Outline every Plasmodium parasite.
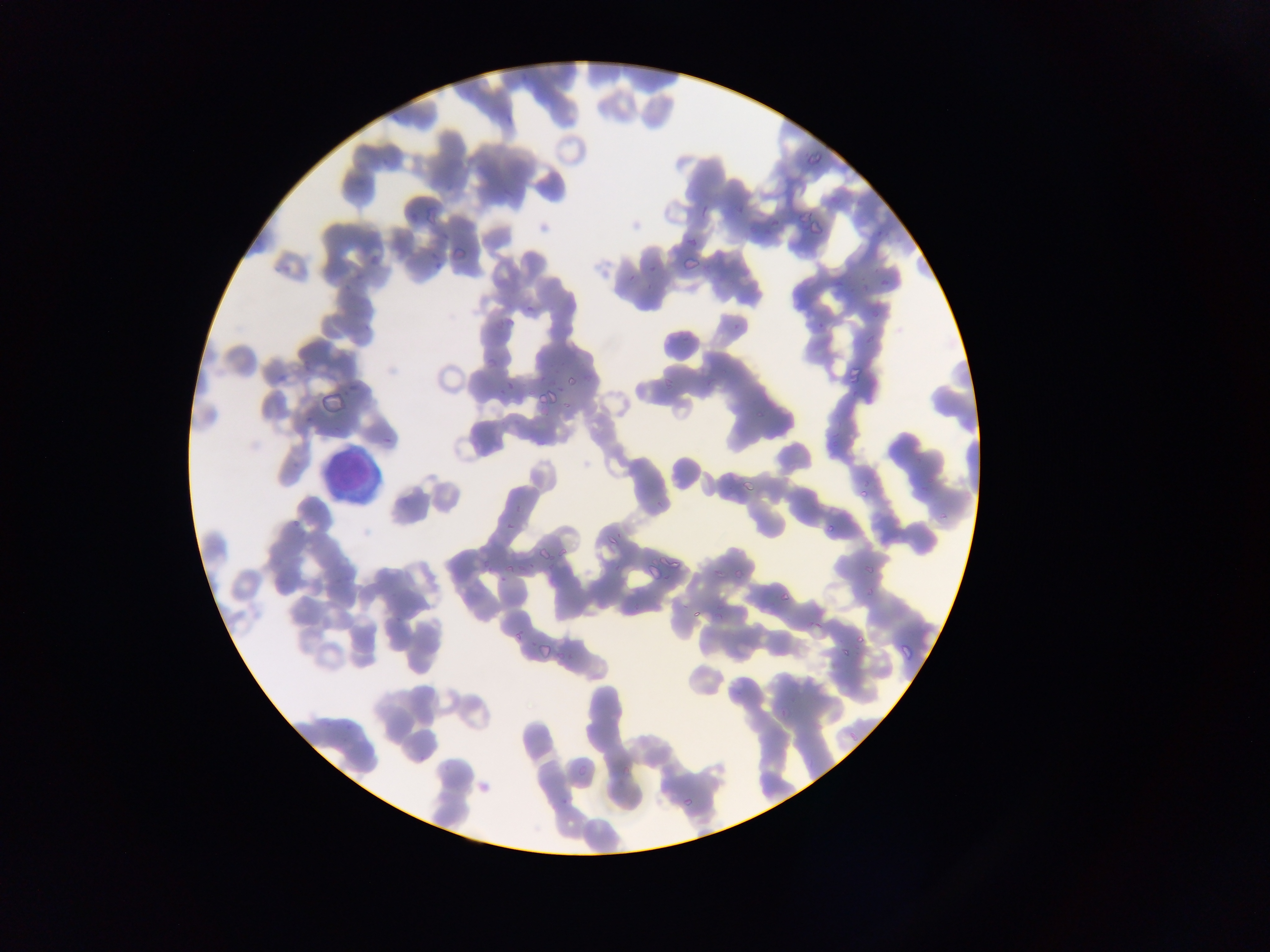

Approximate bounding boxes as [left, top, right, bottom] in pixels.
Plasmodium parasites: [802, 156, 824, 172], [693, 196, 715, 216], [797, 197, 818, 226], [853, 199, 864, 213], [422, 200, 443, 223], [728, 202, 747, 221], [804, 209, 824, 246], [763, 218, 782, 235], [868, 225, 893, 249], [449, 235, 472, 261], [684, 236, 696, 251], [363, 246, 382, 265], [425, 247, 442, 268], [681, 251, 699, 273], [647, 258, 664, 275], [623, 268, 644, 284], [876, 268, 896, 295], [523, 299, 544, 324], [860, 299, 884, 328], [813, 312, 833, 329], [498, 318, 509, 329], [727, 318, 747, 331], [676, 331, 694, 345], [484, 354, 497, 370], [275, 364, 292, 386], [837, 366, 866, 399], [566, 372, 584, 389], [497, 378, 513, 398], [539, 390, 553, 407], [323, 394, 345, 414], [296, 413, 311, 427], [381, 430, 398, 448], [732, 477, 761, 499], [918, 482, 931, 494], [856, 483, 875, 497], [501, 508, 522, 541], [289, 511, 306, 532], [824, 517, 840, 538], [606, 530, 621, 546], [539, 541, 554, 562], [664, 553, 692, 569], [483, 555, 498, 571], [522, 556, 538, 573], [861, 560, 879, 575], [647, 561, 663, 577], [707, 562, 724, 583], [732, 562, 744, 586], [499, 566, 513, 586], [856, 579, 883, 599], [778, 584, 791, 604], [712, 600, 724, 621], [390, 603, 407, 627], [685, 605, 700, 626], [512, 621, 528, 643], [856, 628, 869, 646], [534, 637, 558, 665], [830, 639, 851, 660], [896, 642, 913, 665], [558, 793, 571, 810], [681, 795, 700, 809] | approximate [x, y] pixel centers of objects too small to bound: [779, 714].

Summary:
  - Leukocyte locations: [315, 445, 383, 509]
  - Preparation: thin blood film
  - Country: Ghana
  - Image size: 1270×952 pixels
  - Capture: mobile-phone photograph through a microscope
  - Field of view: single